Classify this cell by malaria status.
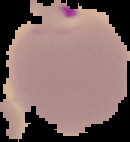

Parasitized.

From a thin blood smear. Image is 130×142 pixels. The area outside the segmented cell region is set to black.